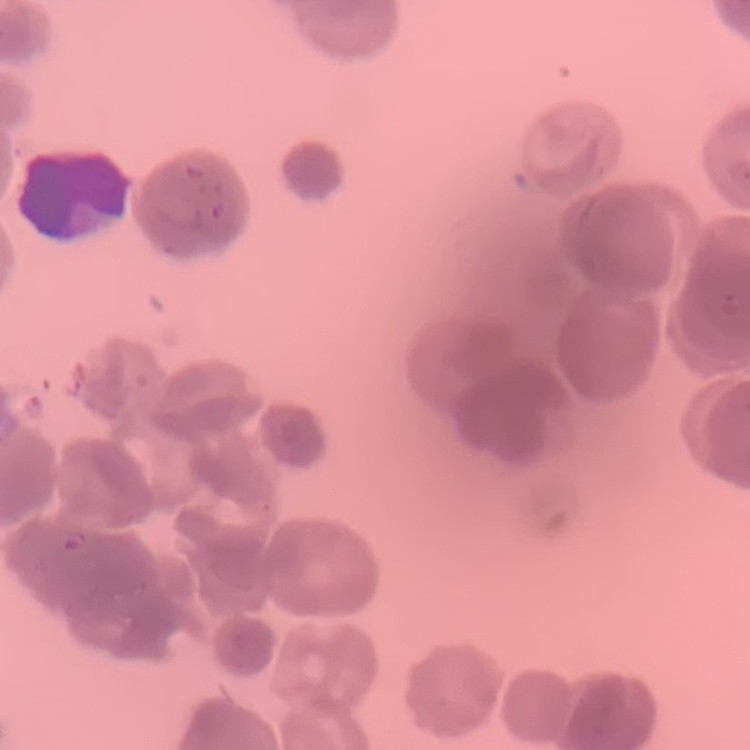 The red blood cells show rouleaux formation. Stained with either Field's or Giemsa. Thin peripheral smear. One tile cut from a larger photomicrograph.